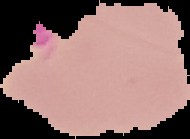 Image is 190×139 pixels. Cell region segmented out of the field of view; the surrounding area is masked to black. From a thin blood film. Malaria status: uninfected.